Outline each Babesia divergens-infected red blood cell.
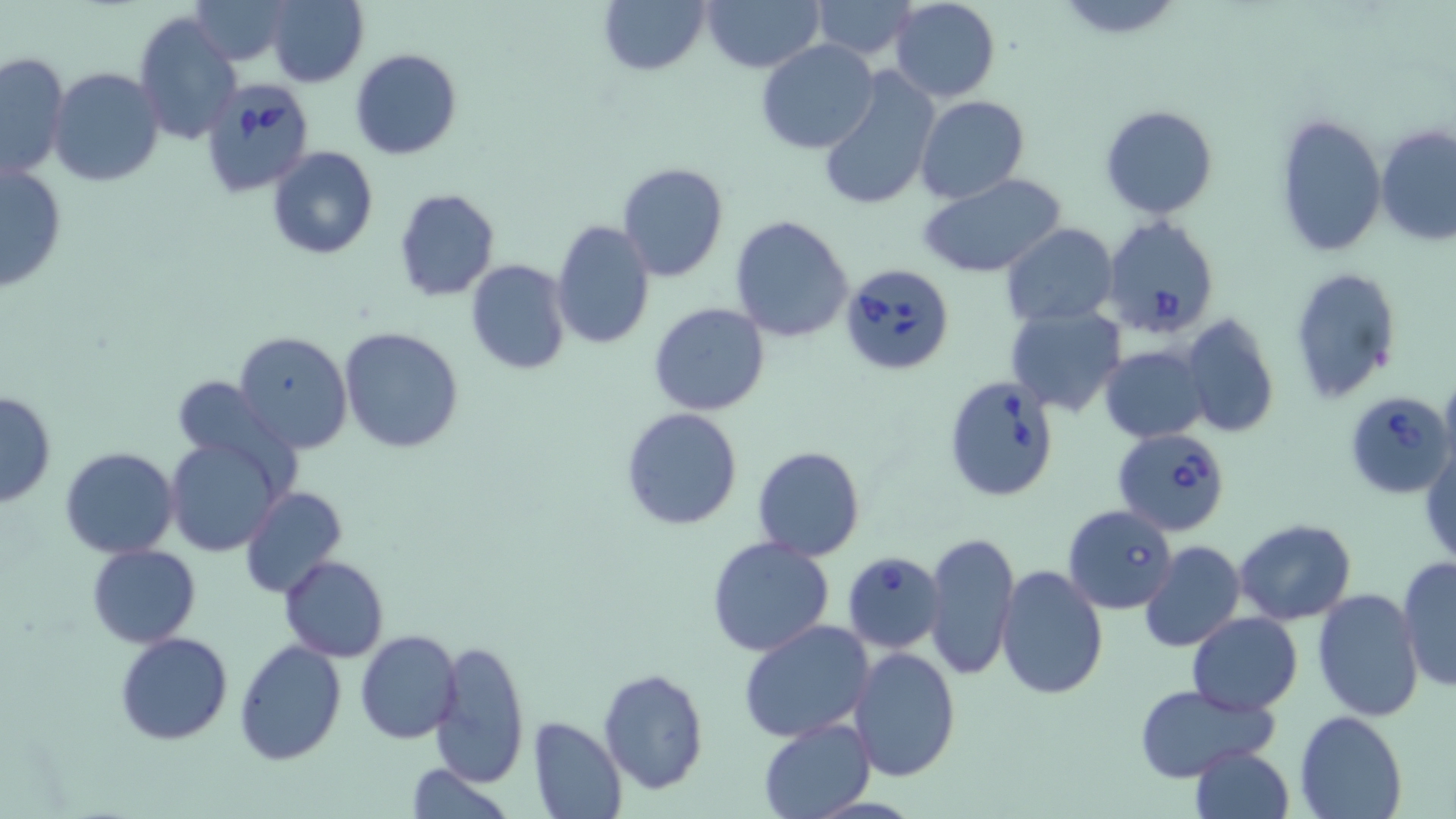
Approximate bounding boxes as [x1, y1, x2, y2] in pixels.
Babesia divergens-infected red blood cells: [200, 81, 313, 199], [1101, 214, 1221, 339], [840, 263, 956, 375], [942, 373, 1062, 502], [1341, 390, 1456, 498], [1112, 427, 1231, 538], [1064, 505, 1178, 614], [843, 551, 947, 655].

Summary:
  - Uninfected red blood cell locations: [188, 0, 294, 64], [266, 0, 368, 88], [597, 0, 712, 75], [700, 0, 823, 72], [811, 0, 919, 60], [890, 0, 1000, 102], [134, 11, 243, 147], [756, 39, 880, 154], [350, 49, 461, 160], [0, 51, 71, 179], [49, 67, 163, 187], [817, 69, 942, 211], [916, 95, 1029, 203], [1099, 104, 1218, 219], [1274, 110, 1389, 258], [1376, 125, 1456, 245], [266, 146, 378, 260], [0, 160, 69, 293], [616, 162, 731, 283], [918, 173, 1067, 280], [392, 189, 500, 301], [730, 215, 855, 341], [549, 220, 656, 351], [1001, 223, 1119, 328], [465, 259, 571, 375], [1289, 266, 1402, 406], [649, 303, 771, 417], [1005, 304, 1127, 416], [1180, 315, 1280, 439], [337, 326, 465, 454], [234, 331, 354, 453], [1100, 344, 1210, 443], [171, 375, 285, 468], [0, 391, 57, 509], [622, 408, 744, 531], [165, 435, 289, 558], [1421, 441, 1456, 568], [753, 446, 865, 561], [60, 447, 179, 559], [242, 485, 347, 599], [1234, 518, 1357, 626], [922, 532, 1019, 677], [706, 536, 835, 658], [1139, 541, 1246, 654], [86, 544, 201, 648], [279, 555, 388, 662], [1398, 557, 1456, 691], [993, 566, 1109, 701], [1312, 587, 1427, 723], [1188, 613, 1303, 713], [739, 619, 876, 742], [355, 631, 462, 743], [116, 632, 234, 745], [430, 637, 531, 789], [232, 638, 348, 769], [848, 647, 962, 781], [597, 668, 710, 794], [1132, 683, 1278, 781], [1295, 708, 1409, 819], [528, 716, 625, 819], [756, 717, 874, 818], [1189, 743, 1296, 819], [402, 762, 517, 819]
  - Slide-level diagnosis: Babesia divergens
  - Field of view: single
  - Preparation: thin blood film
  - Stain: May-Grünwald-Giemsa
  - Modality: optical microscopy
  - Image size: 1456×819 pixels
  - Magnification: 1000x